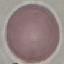

Summary:
  - Malaria status: uninfected
  - Capture: smartphone through the microscope eyepiece
  - Stain: Giemsa
  - Image type: automatically extracted cell patch, resized to 64 × 64 pixels
  - Preparation: thin smear